Assess this cell for malaria.
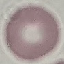

Uninfected.

Acquired by smartphone through the microscope eyepiece. Giemsa-stained preparation. Cell patch, automatically extracted from a larger field of view and resized to 64 × 64 pixels. Thin blood film.